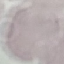 Result: no malaria parasites seen. Photographed with a smartphone camera at the microscope eyepiece. Thin blood film. Automatically extracted cell patch, resized to 64 × 64 pixels. Giemsa stain.